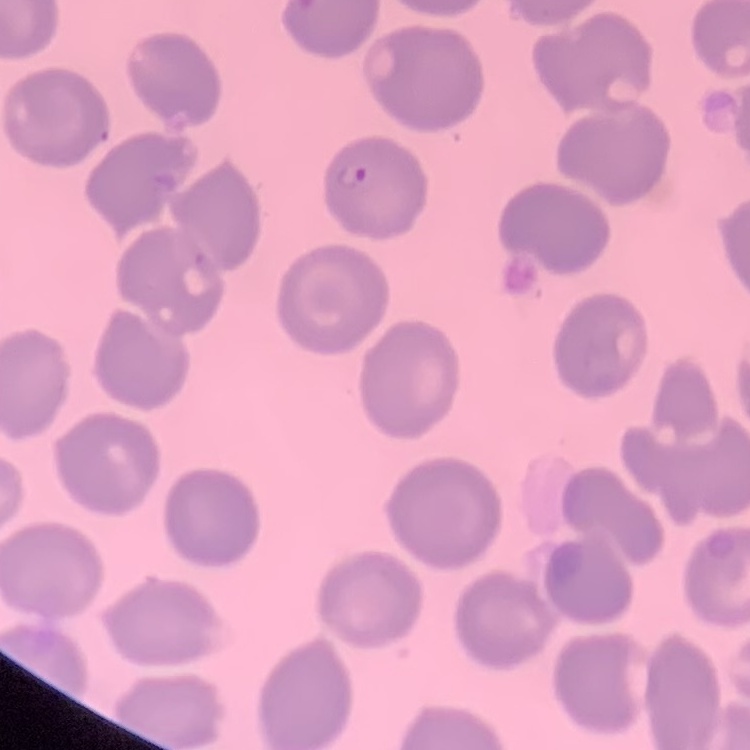

The erythrocytes show no rouleaux formation. Thin blood smear. Field's or Giemsa stain. One tile cut from a larger photomicrograph.